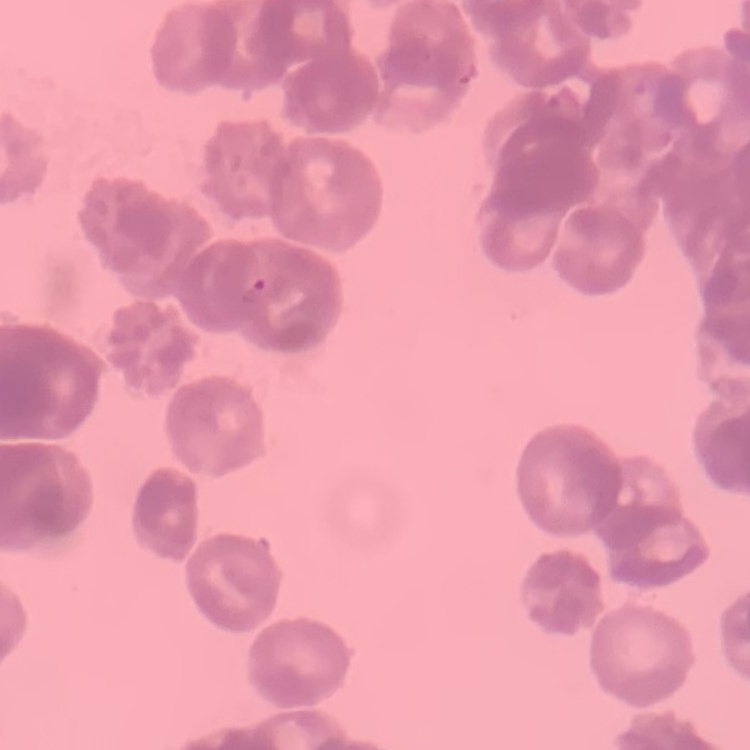
red blood cell morphology = rouleaux formation
image type = square crop of a larger photomicrograph
preparation = thin blood smear
stain = Field's or Giemsa